Give the preparation type.
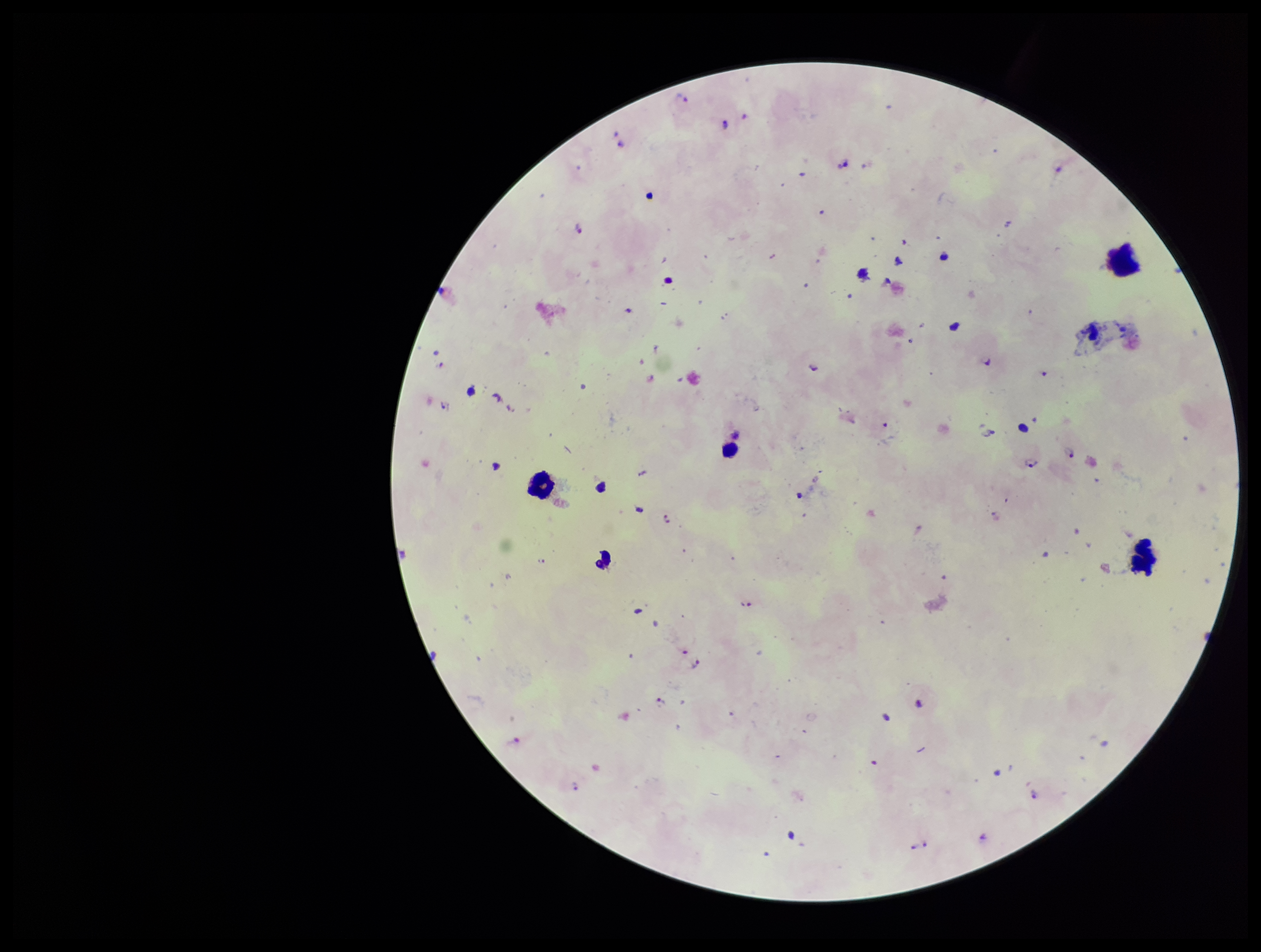

A thick smear.

Summary:
  - Capture: smartphone photograph through the microscope eyepiece
  - Plasmodium parasites: seen
  - Image size: 1261×952 pixels
  - Field of view: single
  - Parasite count: 16
  - Patient malaria status: infected
  - Stain: Giemsa
  - Leukocyte count: 4
  - Species reported for this patient: Plasmodium falciparum